Locate every leukocyte (white blood cell).
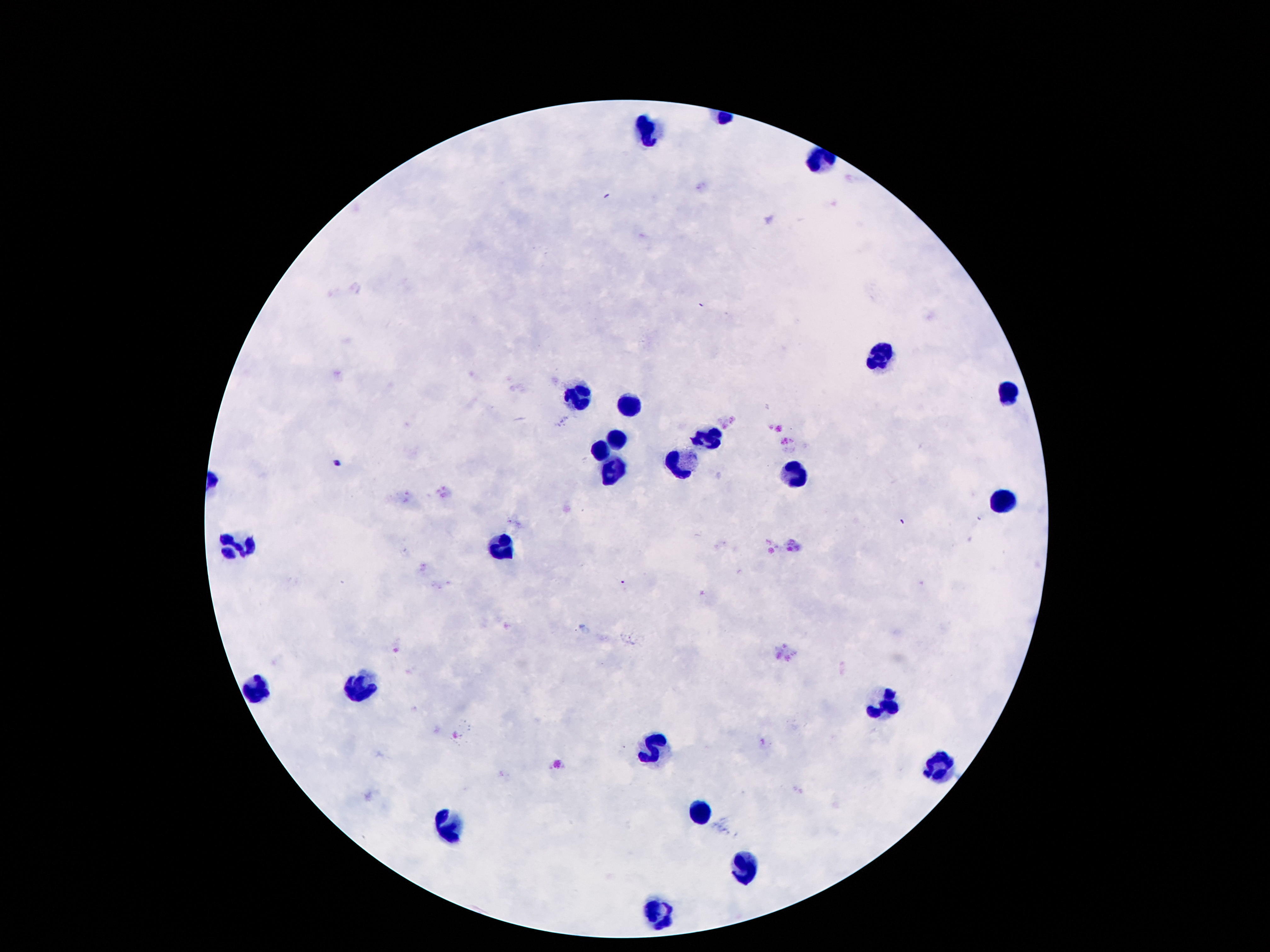
Approximate centers as (x, y) in pixels.
Leukocytes: (649, 127), (878, 355), (1006, 393), (574, 397), (628, 409), (619, 437), (705, 440), (602, 451), (682, 466), (614, 470), (791, 474), (999, 500), (236, 545), (504, 547), (259, 689), (355, 689), (888, 705), (653, 747), (940, 764), (699, 811), (450, 820), (741, 866), (658, 911).

Summary:
  - Magnification: 100x
  - Stain: Giemsa
  - Patient malaria status: not infected
  - Capture: smartphone camera through the microscope eyepiece
  - Preparation: thick blood smear
  - Image size: 1270×952 pixels
  - Field of view: one from this slide